Assess this cell for malaria.
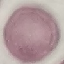

Uninfected.

Giemsa stain. Acquired by smartphone through the microscope eyepiece. Thin smear of blood. Automatically extracted cell patch, resized to 64 × 64 pixels.